Locate every blood parasite and identify its species.
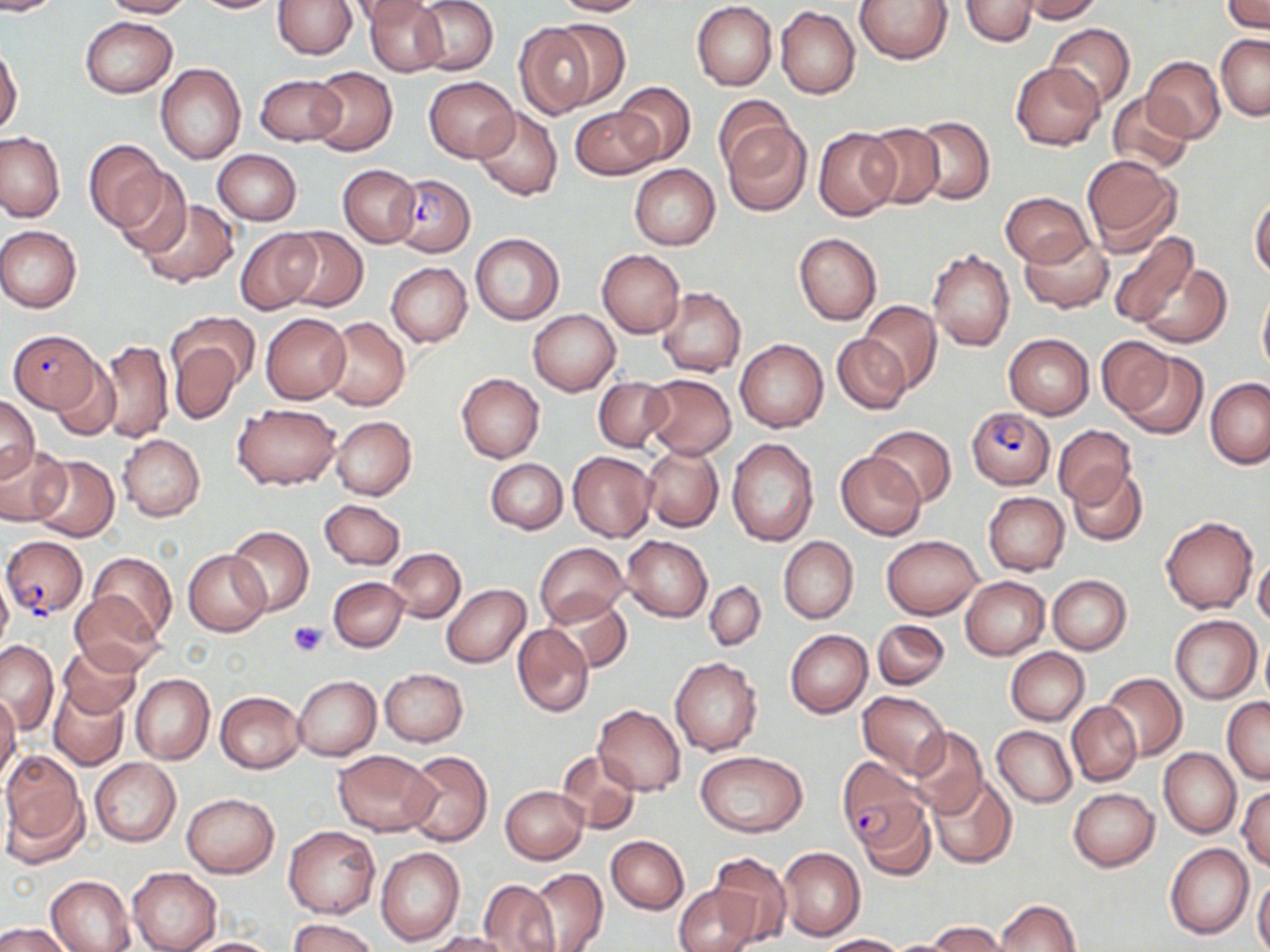

Approximate bounding boxes as (x1,y1)-(x2,y2) corner pairs in pixels.
Plasmodium falciparum-infected red blood cells: (392,172)-(475,256), (7,330)-(103,413), (966,407)-(1056,487), (3,537)-(86,618), (837,759)-(931,860).
No Plasmodium ovale, Plasmodium malariae, Plasmodium vivax, Babesia divergens, or Trypanosoma brucei observed.

Uninfected red blood cell locations: (0,0)-(59,15), (99,0)-(194,17), (190,0)-(283,14), (348,0)-(434,27), (365,0)-(447,76), (411,0)-(497,76), (550,0)-(645,17), (855,0)-(954,64), (961,0)-(1039,47), (1015,0)-(1103,23), (274,1)-(355,59), (692,1)-(777,89), (1223,1)-(1270,33), (775,6)-(860,99), (81,17)-(176,98), (550,19)-(630,108), (513,21)-(602,117), (1045,24)-(1136,109), (1215,33)-(1270,120), (0,45)-(23,137), (1142,56)-(1226,143), (1010,60)-(1104,151), (155,64)-(246,164), (307,66)-(397,157), (255,73)-(346,146), (424,77)-(518,162), (614,81)-(696,167), (1107,91)-(1193,175), (713,95)-(799,175), (571,105)-(664,179), (473,107)-(562,200), (908,115)-(995,204), (721,121)-(811,216), (859,123)-(945,209), (814,127)-(899,221), (0,132)-(64,222), (83,140)-(168,233), (213,149)-(301,224), (1081,154)-(1182,256), (628,164)-(720,250), (338,165)-(420,247), (110,169)-(191,258), (1000,192)-(1093,266), (1251,194)-(1270,280), (137,200)-(239,287), (0,225)-(82,313), (282,227)-(367,312), (235,229)-(320,314), (1104,230)-(1199,331), (1020,231)-(1112,312), (794,232)-(882,325), (469,233)-(564,325), (927,247)-(1015,352), (596,248)-(685,336), (1134,261)-(1230,348), (386,263)-(472,347), (1257,284)-(1270,381), (656,287)-(746,377), (858,301)-(944,393), (528,309)-(619,396), (170,311)-(259,392), (261,313)-(351,404), (322,316)-(409,411), (832,334)-(910,414), (1004,334)-(1095,418), (1096,336)-(1177,420), (170,338)-(242,424), (735,338)-(828,432), (98,339)-(173,444), (1117,350)-(1207,439), (51,359)-(120,441), (456,373)-(544,462), (641,373)-(736,459), (594,376)-(673,452), (1204,377)-(1270,467), (1,392)-(39,484), (233,402)-(341,489), (330,416)-(416,500), (1053,424)-(1137,507), (866,425)-(956,506), (118,433)-(205,521), (726,438)-(818,545), (0,444)-(71,526), (641,445)-(724,533), (567,451)-(657,541), (835,452)-(927,540), (29,455)-(119,541), (486,459)-(567,534), (1068,464)-(1148,546), (983,492)-(1069,575), (318,499)-(405,569), (1161,517)-(1258,614), (226,526)-(314,615), (882,534)-(983,619), (622,535)-(713,621), (778,535)-(858,623), (534,542)-(629,627), (387,548)-(466,622), (183,549)-(270,636), (87,551)-(177,642), (1253,552)-(1270,628), (0,570)-(13,658), (1047,574)-(1132,653), (960,576)-(1049,659), (328,577)-(408,651), (704,580)-(765,650), (441,584)-(530,668), (69,590)-(166,673), (544,594)-(631,673), (1169,615)-(1261,703), (872,619)-(948,690), (511,624)-(595,718), (785,629)-(873,718), (1259,634)-(1270,704), (0,639)-(57,734), (60,643)-(141,718), (1006,648)-(1089,725), (670,657)-(764,756), (379,668)-(469,746), (1101,672)-(1186,762), (130,674)-(215,764), (295,676)-(380,760), (49,683)-(130,770), (858,690)-(949,777), (216,691)-(306,772), (0,692)-(21,785), (1222,696)-(1270,785), (1067,701)-(1141,786), (594,705)-(685,796), (905,725)-(989,818), (993,725)-(1077,807), (1158,748)-(1240,839), (401,749)-(493,846), (331,750)-(438,836), (554,750)-(640,834), (695,751)-(807,836), (0,752)-(89,864), (89,757)-(180,846), (929,775)-(1016,868), (501,785)-(587,863), (1236,786)-(1270,871), (1069,787)-(1158,871), (181,792)-(279,877), (858,798)-(936,880), (283,825)-(380,918), (606,836)-(688,915), (1165,843)-(1253,940), (777,846)-(865,941), (375,847)-(464,946), (710,851)-(790,944), (128,866)-(222,951), (525,868)-(607,951), (45,875)-(135,952), (1252,877)-(1270,952), (479,878)-(560,952), (673,883)-(761,952), (994,899)-(1080,951), (288,918)-(378,952), (927,921)-(1006,951), (0,923)-(74,952), (427,931)-(516,952), (818,934)-(905,951), (179,937)-(282,952), (878,938)-(967,951). Platelet locations: (289,620)-(327,657). Slide-level diagnosis: Plasmodium falciparum. One field of a larger specimen. May-Grünwald-Giemsa stain. Thin blood film. Optical microscopy. 1000x magnification. Image is 1270×952 pixels.